State which parasite is depicted.
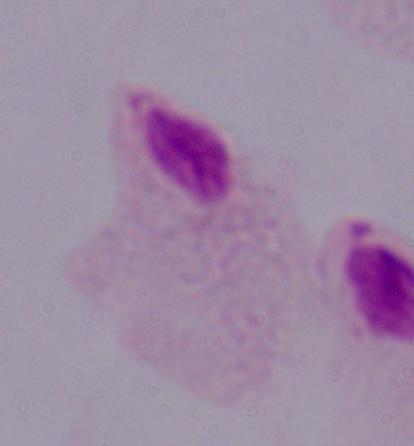
A trichomonad.

magnification = 1000x
modality = photomicrograph